Report the malaria status of this cell.
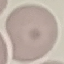

It is uninfected.

{
  "capture": "smartphone camera at the microscope eyepiece",
  "stain": "Giemsa",
  "preparation": "thin blood smear",
  "image_type": "automatically extracted cell patch, resized to 64 × 64 pixels"
}